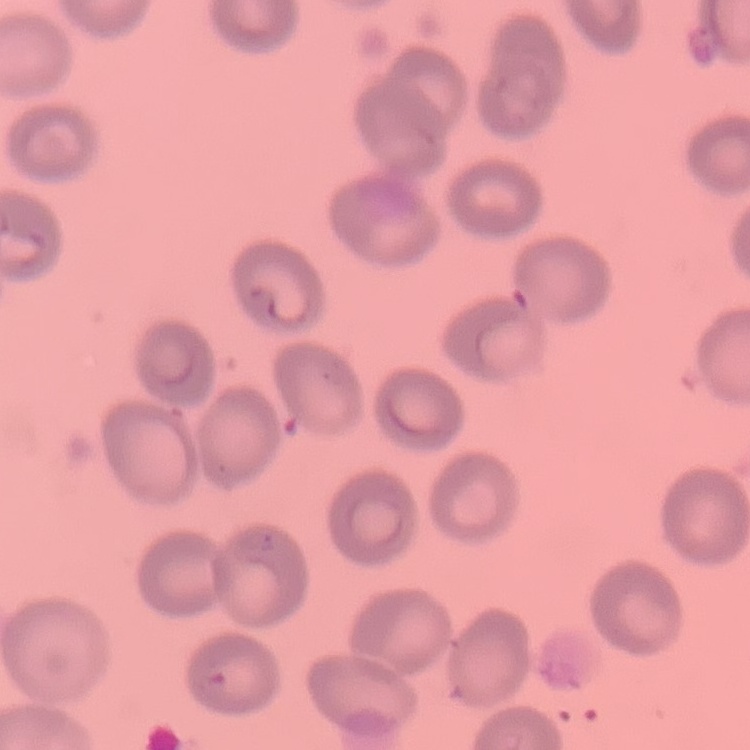

Summary:
  - Erythrocyte morphology: no rouleaux formation
  - Stain: Field's or Giemsa
  - Preparation: thin blood film
  - Image type: one tile cut from a larger photomicrograph